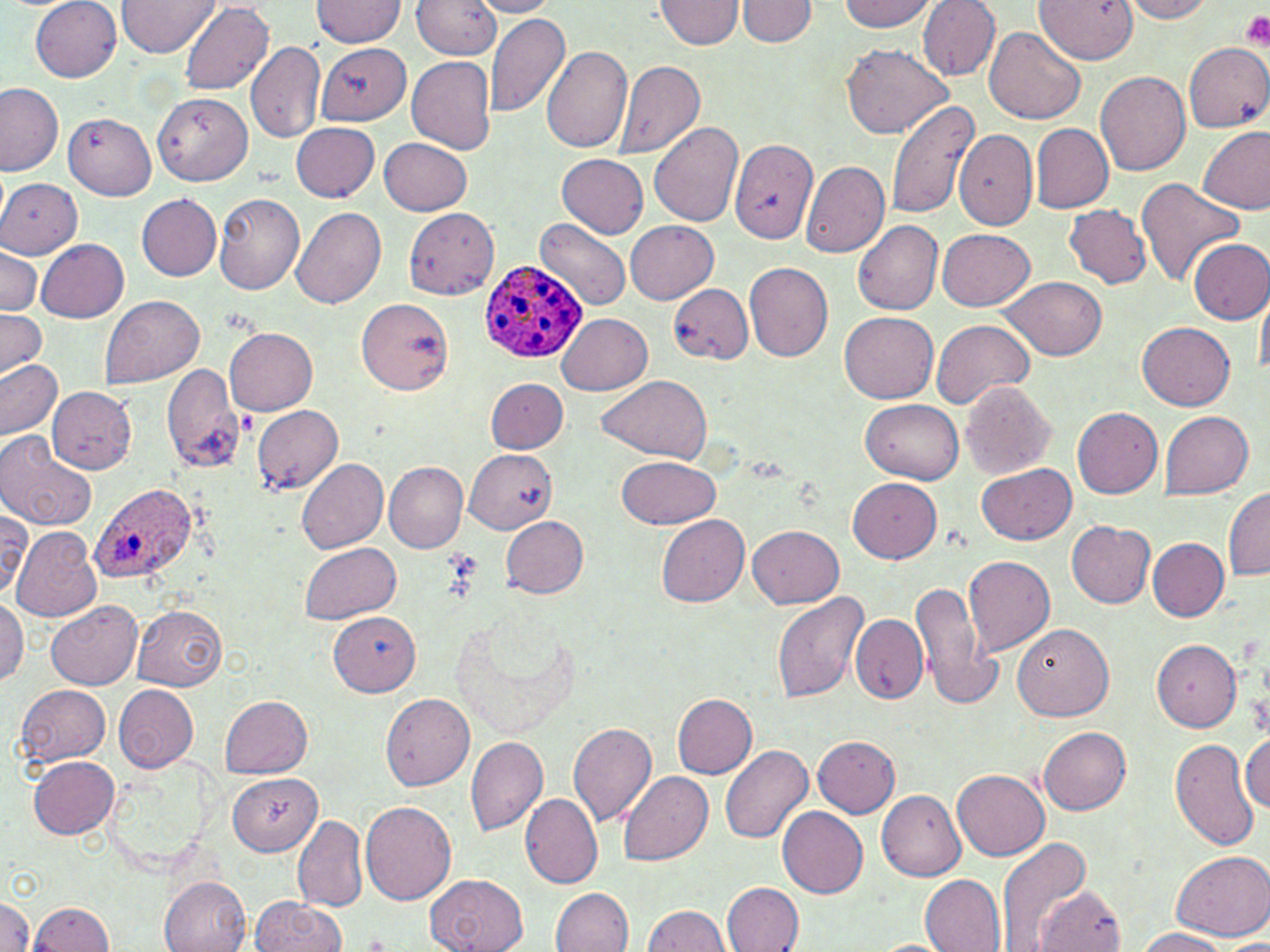

Plasmodium ovale-infected red blood cell locations = approximate bounding boxes as [x1, y1, x2, y2] in pixels: [481, 255, 584, 364], [89, 484, 194, 584]
slide-level diagnosis = Plasmodium ovale
preparation = thin blood film
field of view = one of a larger specimen
modality = optical microscopy
stain = May-Grünwald-Giemsa
uninfected red blood cell locations = approximate bounding boxes as [x1, y1, x2, y2] in pixels: [31, 0, 123, 81], [117, 0, 217, 56], [311, 0, 406, 47], [412, 0, 501, 59], [470, 0, 561, 17], [657, 0, 746, 49], [737, 0, 817, 46], [836, 0, 936, 32], [1034, 0, 1139, 64], [1120, 0, 1218, 21], [915, 1, 1001, 82], [178, 2, 274, 95], [486, 11, 571, 119], [985, 26, 1087, 124], [245, 41, 326, 142], [839, 41, 954, 138], [316, 42, 411, 126], [1182, 42, 1270, 133], [542, 46, 633, 155], [406, 57, 497, 153], [613, 59, 706, 160], [1096, 71, 1192, 176], [0, 83, 64, 176], [153, 93, 251, 184], [885, 100, 982, 221], [63, 114, 156, 199], [649, 121, 745, 227], [291, 123, 378, 201], [1031, 124, 1113, 212], [1197, 125, 1270, 214], [954, 128, 1037, 230], [379, 137, 471, 214], [731, 140, 818, 244], [557, 155, 650, 238], [800, 161, 890, 258], [1136, 178, 1247, 286], [0, 179, 81, 257], [213, 192, 305, 295], [135, 193, 221, 279], [1064, 205, 1151, 289], [291, 207, 386, 310], [403, 207, 499, 298], [534, 217, 630, 313], [852, 218, 943, 315], [625, 220, 718, 305], [937, 229, 1035, 311], [1188, 237, 1270, 324], [36, 239, 129, 322], [0, 244, 40, 316], [743, 261, 834, 362], [1002, 276, 1109, 360], [668, 284, 752, 364], [1256, 285, 1270, 383], [101, 295, 204, 390], [357, 297, 454, 394], [0, 309, 47, 378], [839, 311, 938, 404], [556, 313, 652, 396], [932, 319, 1034, 407], [1138, 321, 1235, 408], [225, 328, 318, 415], [0, 358, 62, 440], [162, 363, 244, 477], [597, 375, 711, 462], [486, 379, 567, 452], [958, 381, 1059, 478], [47, 386, 137, 474], [861, 397, 963, 483], [253, 404, 343, 493], [1073, 407, 1163, 498], [1159, 411, 1254, 498], [1, 436, 96, 532], [465, 449, 557, 532], [296, 455, 388, 554], [617, 455, 719, 530], [384, 462, 467, 552], [977, 463, 1076, 545], [848, 477, 942, 563], [1224, 486, 1270, 579], [0, 507, 32, 596], [657, 515, 749, 607], [500, 516, 589, 598], [1066, 520, 1155, 609], [747, 525, 843, 609], [12, 527, 101, 622], [1146, 537, 1229, 621], [298, 542, 401, 624], [963, 555, 1055, 658], [910, 574, 997, 710], [769, 591, 869, 703], [0, 596, 28, 686], [44, 600, 142, 691], [132, 606, 227, 690], [329, 612, 420, 695], [851, 613, 927, 704], [454, 616, 581, 737], [1013, 625, 1114, 721], [1151, 638, 1241, 733], [113, 683, 199, 771], [15, 684, 109, 766], [381, 693, 475, 790], [673, 693, 757, 778], [219, 694, 313, 778], [567, 718, 658, 828], [1038, 727, 1131, 814], [1241, 733, 1270, 812], [464, 735, 547, 834], [813, 736, 900, 816], [1170, 738, 1261, 852], [720, 744, 813, 847], [26, 755, 119, 839], [953, 769, 1050, 862], [617, 770, 713, 865], [230, 773, 322, 854], [877, 790, 967, 881], [519, 793, 602, 889], [360, 801, 457, 905], [776, 807, 868, 897], [291, 813, 367, 912], [996, 838, 1093, 950], [1168, 849, 1267, 941], [919, 873, 1007, 951], [426, 874, 527, 952], [158, 875, 250, 952], [724, 882, 804, 952], [1033, 885, 1125, 952], [551, 888, 633, 952], [249, 895, 343, 952], [0, 896, 35, 951], [28, 901, 115, 952], [641, 905, 733, 952], [1133, 927, 1230, 952]
image size = 1270×952 pixels
magnification = 1000x
platelet locations = approximate bounding boxes as [x1, y1, x2, y2] in pixels: [1241, 10, 1270, 49], [242, 410, 257, 434]